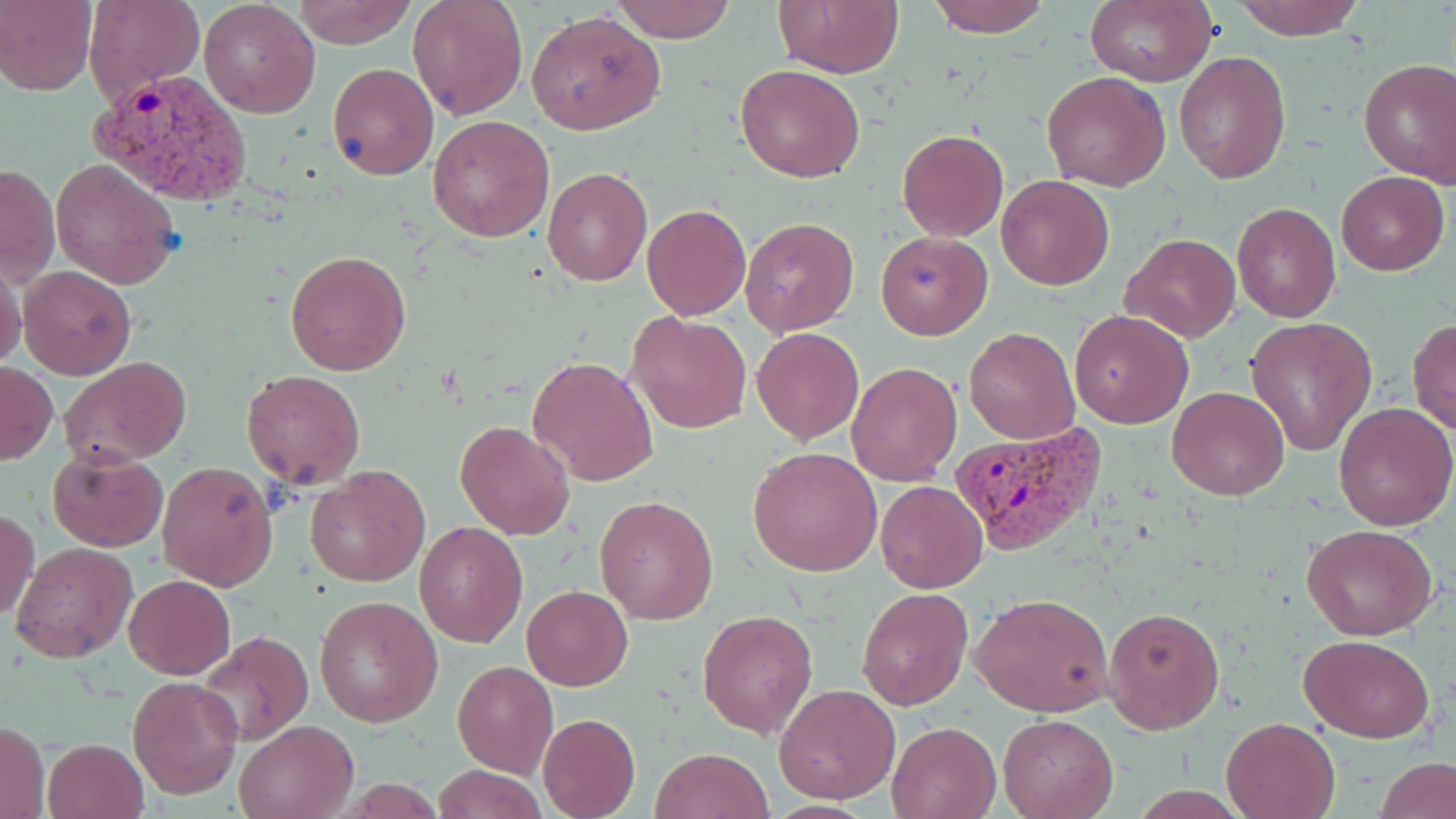 Approximate bounding boxes as (x1, y1, x2, y2) in pixels. Uninfected red blood cell locations: (82, 0, 203, 108), (292, 0, 418, 48), (408, 0, 527, 120), (612, 0, 737, 43), (777, 0, 903, 78), (926, 0, 1052, 39), (1229, 0, 1366, 41), (0, 1, 97, 94), (1084, 1, 1217, 86), (199, 2, 321, 118), (527, 11, 664, 136), (1173, 50, 1291, 184), (1359, 60, 1456, 187), (328, 63, 438, 180), (736, 63, 866, 183), (1042, 71, 1169, 191), (427, 114, 555, 243), (897, 130, 1008, 241), (50, 156, 182, 288), (1, 162, 59, 286), (542, 168, 651, 285), (1335, 171, 1449, 275), (997, 175, 1114, 290), (1232, 202, 1340, 322), (642, 204, 751, 319), (738, 216, 859, 338), (876, 231, 992, 339), (1120, 232, 1239, 343), (285, 248, 412, 376), (0, 258, 26, 374), (18, 264, 136, 379), (626, 309, 752, 434), (1070, 309, 1194, 429), (1245, 317, 1377, 454), (1407, 317, 1456, 436), (751, 326, 864, 445), (965, 327, 1080, 444), (527, 356, 657, 488), (59, 357, 192, 468), (0, 362, 57, 466), (847, 362, 961, 484), (240, 369, 366, 488), (1168, 386, 1290, 499), (1333, 403, 1456, 531), (456, 420, 574, 539), (48, 447, 168, 551), (748, 447, 882, 576), (156, 459, 278, 590), (307, 465, 430, 587), (876, 480, 987, 594), (595, 494, 718, 625), (1, 507, 41, 621), (414, 520, 528, 649), (1302, 525, 1440, 640), (13, 542, 138, 662), (123, 573, 236, 679), (522, 585, 632, 690), (857, 588, 972, 711), (972, 593, 1116, 717), (313, 594, 442, 727), (1102, 604, 1226, 736), (698, 609, 819, 739), (195, 630, 312, 745), (1300, 634, 1435, 743), (452, 660, 558, 778), (128, 676, 244, 800), (775, 683, 900, 803), (537, 712, 641, 819), (998, 714, 1118, 818), (1220, 715, 1342, 819), (234, 719, 359, 818), (0, 721, 49, 819), (886, 722, 1000, 818), (42, 738, 148, 819), (651, 747, 774, 819), (1377, 758, 1456, 819), (432, 764, 547, 819). Plasmodium vivax-infected red blood cell locations: (92, 69, 252, 205), (953, 421, 1104, 553). Slide-level diagnosis: Plasmodium vivax. May-Grünwald-Giemsa stain. Thin blood smear. Image is 1456×819 pixels. Light microscopy. 1000x magnification. One field of a larger specimen.